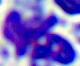

{
  "magnification": "400x",
  "modality": "micrograph",
  "identification": "white blood cell"
}